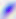

{
  "identification": "Toxoplasma gondii",
  "magnification": "400x",
  "modality": "photomicrograph"
}